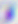

{
  "magnification": "400x",
  "modality": "micrograph",
  "identification": "Toxoplasma gondii"
}